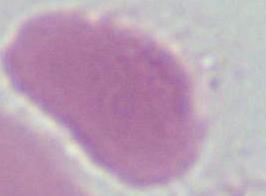 1000x magnification. Micrograph. A red blood cell is seen.